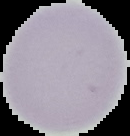

image_size: 130×136 pixels
malaria_status: uninfected
image_type: segmented cell region on a black background
preparation: thin blood smear